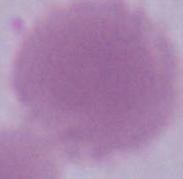
Micrograph. An erythrocyte is shown. 1000x magnification.